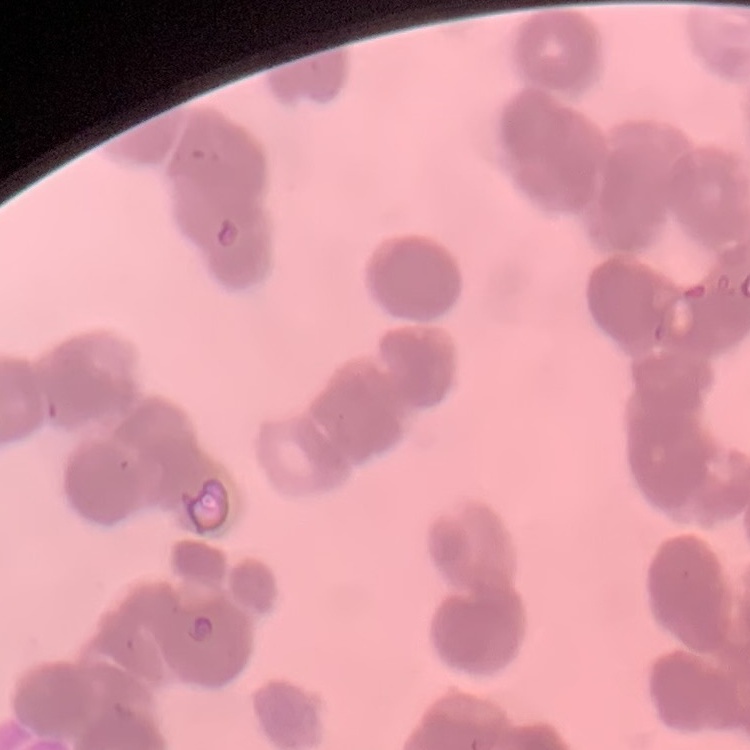

red_blood_cell_morphology: rouleaux formation
preparation: thin peripheral smear
image_type: one tile cut from a larger photomicrograph
stain: Field's or Giemsa